Locate every blood parasite and identify its species.
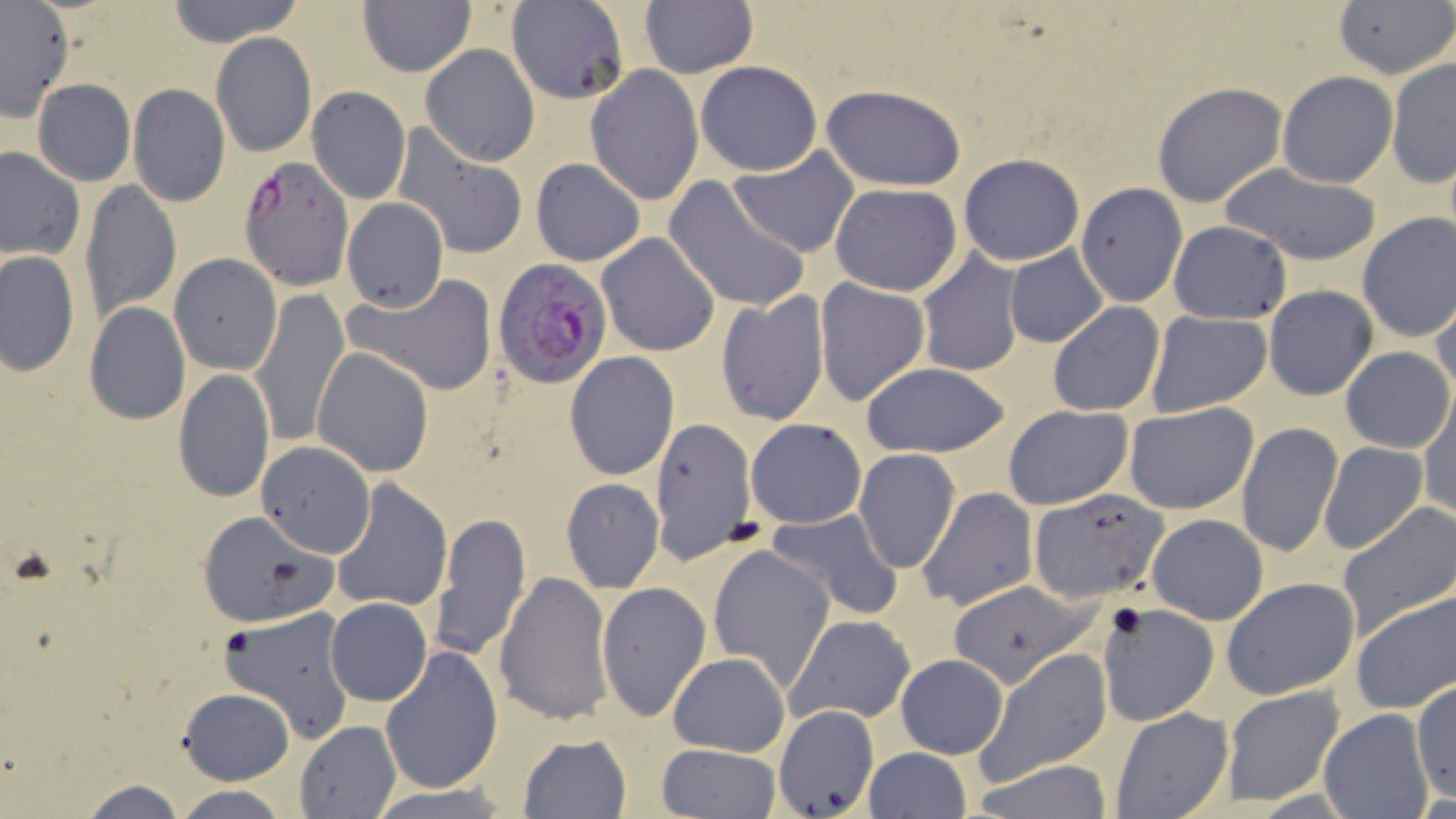

Approximate bounding boxes as [x1, y1, x2, y2] in pixels.
Plasmodium falciparum-infected red blood cells: [239, 155, 354, 288], [493, 259, 611, 388].
No Plasmodium ovale, Plasmodium malariae, Plasmodium vivax, Babesia divergens, or Trypanosoma brucei observed.

Uninfected red blood cell locations: [165, 0, 302, 48], [357, 0, 475, 75], [505, 1, 630, 105], [640, 2, 757, 78], [1333, 2, 1454, 81], [0, 3, 74, 119], [211, 32, 315, 158], [420, 44, 540, 166], [1387, 55, 1455, 189], [694, 61, 823, 176], [584, 66, 705, 204], [1277, 71, 1398, 188], [32, 78, 136, 186], [1152, 82, 1288, 209], [127, 83, 231, 206], [821, 85, 967, 192], [306, 86, 411, 203], [392, 125, 529, 261], [726, 146, 860, 258], [0, 147, 83, 260], [959, 153, 1085, 266], [531, 158, 645, 267], [1217, 164, 1383, 266], [663, 176, 811, 315], [80, 180, 181, 320], [830, 183, 963, 296], [1075, 183, 1187, 307], [342, 196, 449, 312], [1354, 211, 1456, 344], [1168, 220, 1291, 325], [597, 231, 721, 357], [1002, 245, 1110, 349], [915, 250, 1024, 378], [1, 252, 78, 375], [169, 254, 281, 375], [343, 277, 499, 397], [813, 277, 931, 408], [1264, 285, 1378, 401], [1429, 287, 1456, 405], [250, 289, 350, 448], [715, 292, 829, 426], [84, 302, 190, 425], [1046, 302, 1164, 416], [1144, 310, 1272, 416], [1339, 346, 1452, 453], [311, 347, 435, 476], [564, 352, 678, 480], [859, 362, 1011, 458], [174, 367, 274, 504], [1418, 392, 1456, 522], [1124, 401, 1259, 515], [1003, 405, 1130, 511], [746, 418, 866, 528], [649, 421, 757, 559], [1235, 421, 1343, 559], [256, 442, 376, 556], [1319, 442, 1428, 555], [853, 449, 961, 573], [560, 478, 664, 593], [331, 479, 453, 613], [918, 487, 1037, 611], [1026, 487, 1170, 607], [1336, 502, 1456, 642], [768, 506, 905, 620], [431, 511, 531, 662], [1145, 512, 1270, 624], [197, 513, 334, 626], [707, 544, 836, 690], [495, 572, 613, 725], [1222, 577, 1360, 700], [950, 579, 1098, 687], [595, 581, 711, 724], [1350, 590, 1456, 713], [326, 598, 432, 705], [1098, 601, 1221, 727], [220, 606, 355, 743], [785, 614, 917, 724], [379, 643, 504, 797], [976, 647, 1112, 782], [668, 652, 789, 757], [895, 652, 1008, 759], [1412, 681, 1455, 801], [1218, 684, 1347, 807], [178, 689, 294, 784], [772, 703, 879, 818], [1110, 707, 1234, 817], [1318, 709, 1435, 818], [296, 721, 401, 818], [518, 734, 632, 818], [656, 744, 779, 818], [861, 748, 973, 819], [972, 760, 1116, 818], [76, 778, 189, 819], [362, 782, 517, 818], [169, 785, 294, 819]. Slide-level diagnosis: Plasmodium falciparum. May-Grünwald-Giemsa-stained preparation. Thin blood smear. 1000x magnification. Image is 1456×819 pixels. Single field of view. Optical microscopy.